Identify the blood parasite species.
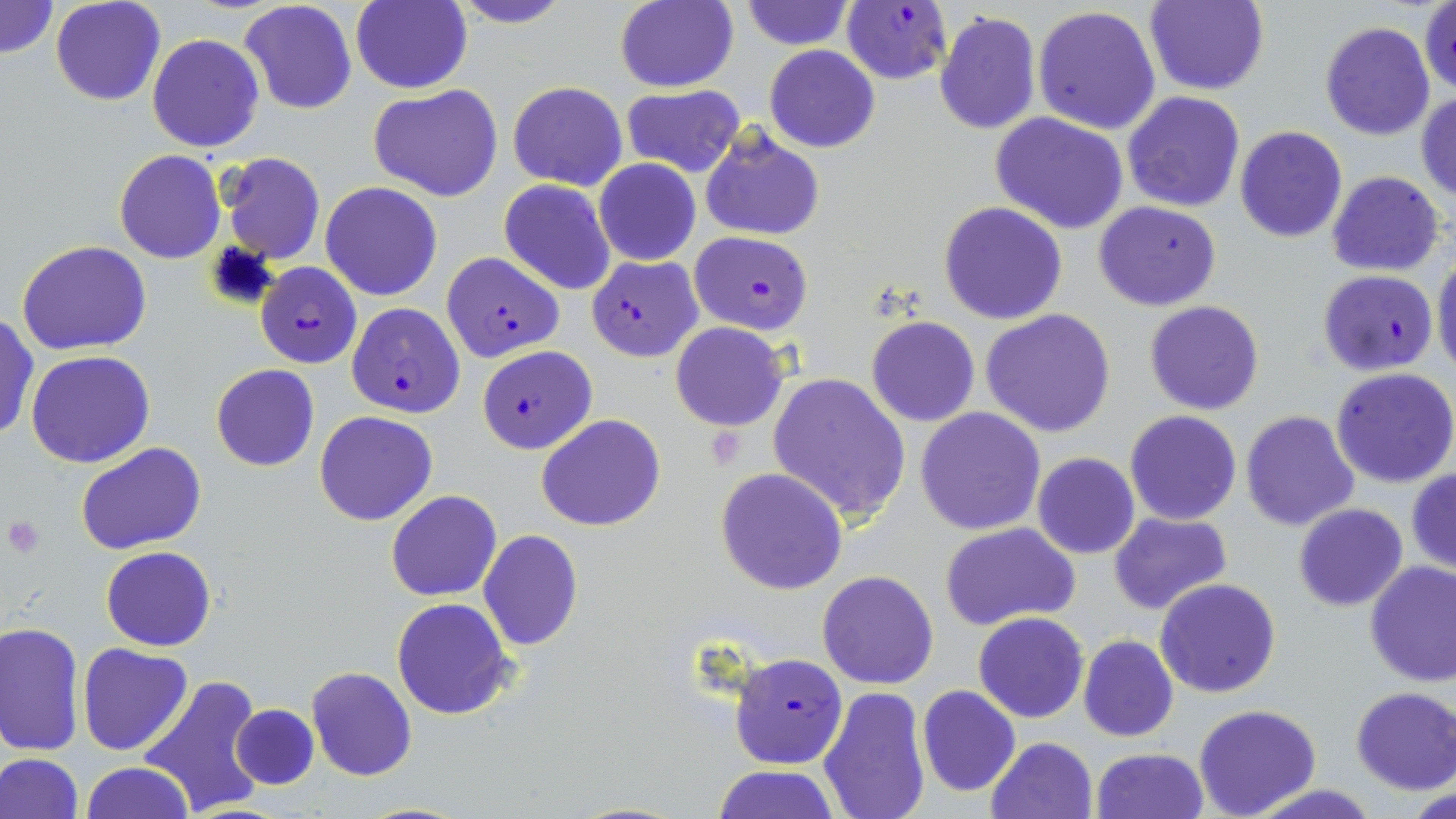

Plasmodium falciparum.

Summary:
  - Coordinate format: approximate bounding boxes as named x1/y1/x2/y2 corners in pixels
  - Platelet locations: (x1=3, y1=515, x2=44, y2=559)
  - Uninfected red blood cell locations: (x1=0, y1=0, x2=58, y2=60), (x1=49, y1=0, x2=165, y2=105), (x1=240, y1=0, x2=358, y2=115), (x1=351, y1=0, x2=471, y2=94), (x1=448, y1=0, x2=574, y2=28), (x1=611, y1=1, x2=739, y2=92), (x1=742, y1=1, x2=853, y2=50), (x1=1146, y1=1, x2=1271, y2=97), (x1=1420, y1=3, x2=1456, y2=96), (x1=1033, y1=6, x2=1162, y2=134), (x1=933, y1=9, x2=1042, y2=137), (x1=1319, y1=21, x2=1435, y2=140), (x1=146, y1=33, x2=265, y2=153), (x1=764, y1=45, x2=880, y2=154), (x1=508, y1=80, x2=628, y2=191), (x1=368, y1=84, x2=505, y2=202), (x1=619, y1=85, x2=745, y2=178), (x1=1121, y1=90, x2=1247, y2=212), (x1=1417, y1=90, x2=1455, y2=202), (x1=991, y1=112, x2=1129, y2=234), (x1=700, y1=127, x2=823, y2=241), (x1=1234, y1=127, x2=1348, y2=243), (x1=114, y1=150, x2=225, y2=263), (x1=217, y1=152, x2=327, y2=265), (x1=594, y1=159, x2=701, y2=266), (x1=1326, y1=170, x2=1446, y2=276), (x1=499, y1=180, x2=615, y2=295), (x1=319, y1=181, x2=444, y2=301), (x1=1093, y1=200, x2=1222, y2=311), (x1=938, y1=201, x2=1067, y2=324), (x1=16, y1=240, x2=152, y2=354), (x1=1433, y1=253, x2=1456, y2=378), (x1=1144, y1=300, x2=1265, y2=415), (x1=981, y1=309, x2=1116, y2=438), (x1=0, y1=313, x2=39, y2=443), (x1=866, y1=316, x2=980, y2=426), (x1=671, y1=322, x2=787, y2=431), (x1=25, y1=350, x2=155, y2=468), (x1=210, y1=363, x2=320, y2=471), (x1=1331, y1=367, x2=1456, y2=487), (x1=766, y1=372, x2=911, y2=525), (x1=915, y1=408, x2=1047, y2=535), (x1=1240, y1=410, x2=1360, y2=532), (x1=314, y1=411, x2=438, y2=526), (x1=1124, y1=411, x2=1243, y2=526), (x1=538, y1=414, x2=665, y2=532), (x1=77, y1=442, x2=206, y2=554), (x1=1032, y1=453, x2=1140, y2=559), (x1=715, y1=467, x2=848, y2=594), (x1=1407, y1=469, x2=1456, y2=574), (x1=386, y1=489, x2=503, y2=601), (x1=1293, y1=503, x2=1408, y2=612), (x1=1108, y1=510, x2=1233, y2=614), (x1=939, y1=522, x2=1082, y2=633), (x1=478, y1=530, x2=584, y2=651), (x1=101, y1=545, x2=216, y2=651), (x1=1363, y1=561, x2=1456, y2=686), (x1=817, y1=570, x2=939, y2=690), (x1=1156, y1=577, x2=1280, y2=697), (x1=390, y1=599, x2=516, y2=720), (x1=972, y1=612, x2=1089, y2=723), (x1=1, y1=621, x2=85, y2=755), (x1=1079, y1=634, x2=1178, y2=741), (x1=78, y1=643, x2=192, y2=756), (x1=305, y1=666, x2=416, y2=781), (x1=137, y1=673, x2=268, y2=818), (x1=917, y1=685, x2=1020, y2=796), (x1=816, y1=686, x2=932, y2=819), (x1=1351, y1=687, x2=1456, y2=795), (x1=230, y1=704, x2=320, y2=790), (x1=1194, y1=705, x2=1322, y2=819), (x1=987, y1=736, x2=1097, y2=819), (x1=1091, y1=747, x2=1208, y2=819), (x1=0, y1=753, x2=85, y2=819), (x1=81, y1=761, x2=193, y2=819), (x1=712, y1=765, x2=839, y2=819), (x1=1252, y1=784, x2=1379, y2=819), (x1=1411, y1=787, x2=1456, y2=819), (x1=570, y1=801, x2=691, y2=818)
  - Plasmodium falciparum-infected red blood cell locations: (x1=842, y1=3, x2=952, y2=85), (x1=690, y1=231, x2=813, y2=334), (x1=440, y1=251, x2=564, y2=362), (x1=586, y1=255, x2=703, y2=362), (x1=255, y1=261, x2=362, y2=367), (x1=1318, y1=269, x2=1438, y2=376), (x1=346, y1=302, x2=465, y2=418), (x1=476, y1=345, x2=596, y2=454), (x1=729, y1=650, x2=848, y2=769)
  - Field of view: single
  - Preparation: thin blood smear
  - Stain: May-Grünwald-Giemsa
  - Modality: light microscopy
  - Image size: 1456×819 pixels
  - Magnification: 1000x